Identify the blood parasite species.
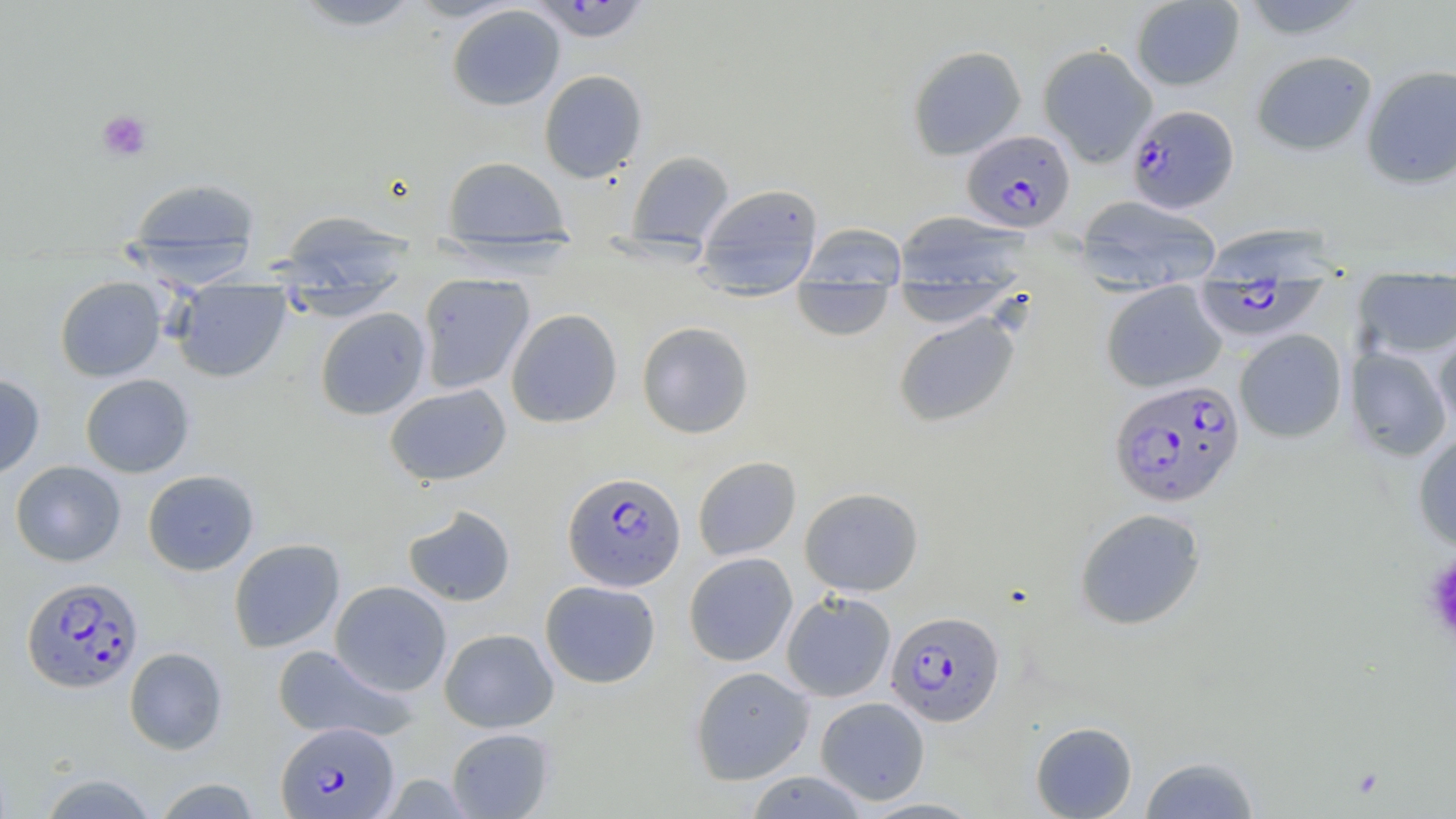

Plasmodium falciparum.

platelet locations = approximate bounding boxes as (x1, y1, x2, y2) in pixels: (96, 109, 153, 162), (1422, 550, 1456, 647)
modality = light microscopy
uninfected red blood cell locations = approximate bounding boxes as (x1, y1, x2, y2) in pixels: (288, 0, 428, 31), (404, 0, 524, 22), (1130, 0, 1245, 91), (1236, 0, 1370, 39), (447, 5, 565, 111), (1038, 44, 1158, 167), (907, 45, 1027, 160), (1251, 50, 1377, 156), (1362, 64, 1456, 189), (539, 69, 648, 183), (627, 150, 734, 247), (442, 156, 570, 242), (126, 176, 261, 270), (694, 182, 825, 293), (1075, 195, 1222, 292), (277, 211, 417, 297), (893, 211, 1030, 291), (799, 223, 908, 287), (1200, 223, 1340, 280), (430, 237, 584, 276), (417, 272, 535, 394), (1352, 273, 1456, 360), (55, 276, 166, 382), (792, 279, 894, 342), (891, 280, 1018, 327), (1101, 280, 1227, 393), (276, 281, 406, 321), (170, 284, 292, 383), (314, 307, 431, 420), (506, 309, 622, 428), (893, 313, 1020, 428), (636, 321, 754, 439), (1433, 323, 1456, 433), (1234, 329, 1347, 443), (1344, 346, 1452, 461), (0, 372, 45, 480), (80, 373, 195, 478), (384, 384, 512, 486), (1412, 432, 1456, 551), (692, 456, 801, 561), (11, 460, 126, 567), (142, 470, 259, 575), (799, 487, 924, 596), (403, 506, 516, 606), (1074, 507, 1207, 631), (229, 538, 345, 653), (684, 552, 798, 666), (330, 580, 452, 696), (540, 580, 661, 688), (781, 591, 896, 702), (438, 628, 558, 733), (271, 644, 415, 744), (124, 647, 228, 754), (689, 666, 815, 785), (815, 696, 930, 805), (1030, 721, 1138, 818), (445, 727, 555, 818), (1139, 755, 1261, 818), (745, 771, 868, 818), (37, 773, 159, 818), (152, 777, 262, 818)
field of view = single
stain = May-Grünwald-Giemsa
Plasmodium falciparum-infected red blood cell locations = approximate bounding boxes as (x1, y1, x2, y2) in pixels: (529, 1, 651, 43), (1126, 104, 1239, 213), (962, 129, 1075, 233), (1194, 279, 1327, 343), (1108, 378, 1245, 508), (562, 471, 686, 592), (21, 575, 143, 693), (885, 610, 1005, 727), (276, 722, 399, 817)
image size = 1456×819 pixels
magnification = 1000x
preparation = thin blood film